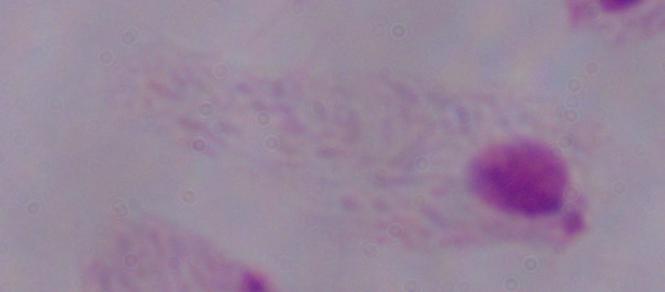
Photomicrograph. A trichomonad is shown. Captured at 1000x magnification.